Assess this cell for malaria.
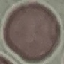
Uninfected.

capture = smartphone through the microscope eyepiece
image type = cell patch, automatically extracted from a larger field of view and resized to 64 × 64 pixels
preparation = thin blood film
stain = Giemsa